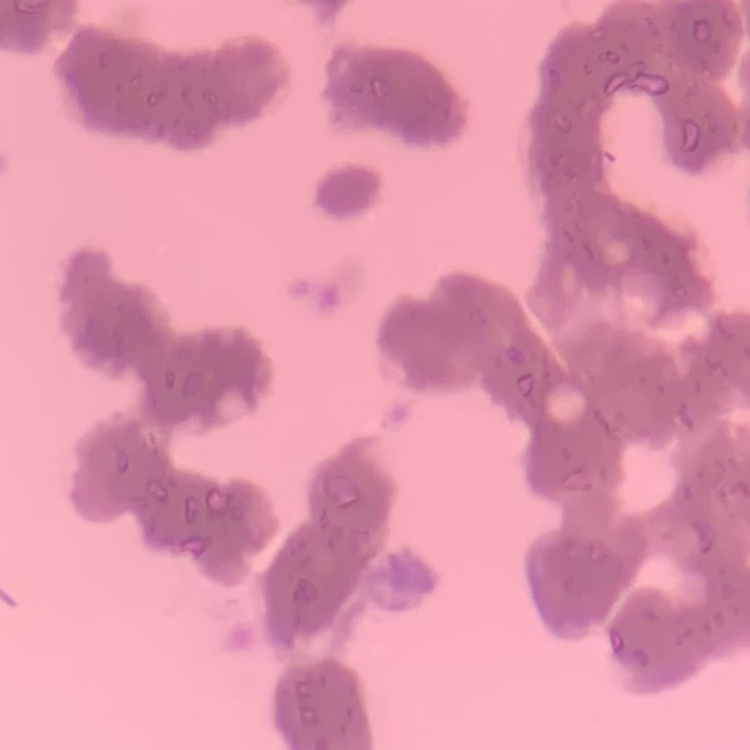
The red blood cells show rouleaux formation. One tile cut from a larger photomicrograph. Thin blood smear. Field's or Giemsa stain.